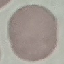

result = no malaria parasites seen
image type = cell patch, automatically extracted from a larger field of view and resized to 64 × 64 pixels
capture = smartphone through the microscope eyepiece
preparation = thin blood smear
stain = Giemsa